Classify this cell by malaria status.
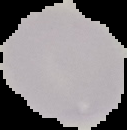
Uninfected.

From a thin blood film. Segmented cell region on a black background. Image is 127×130 pixels.